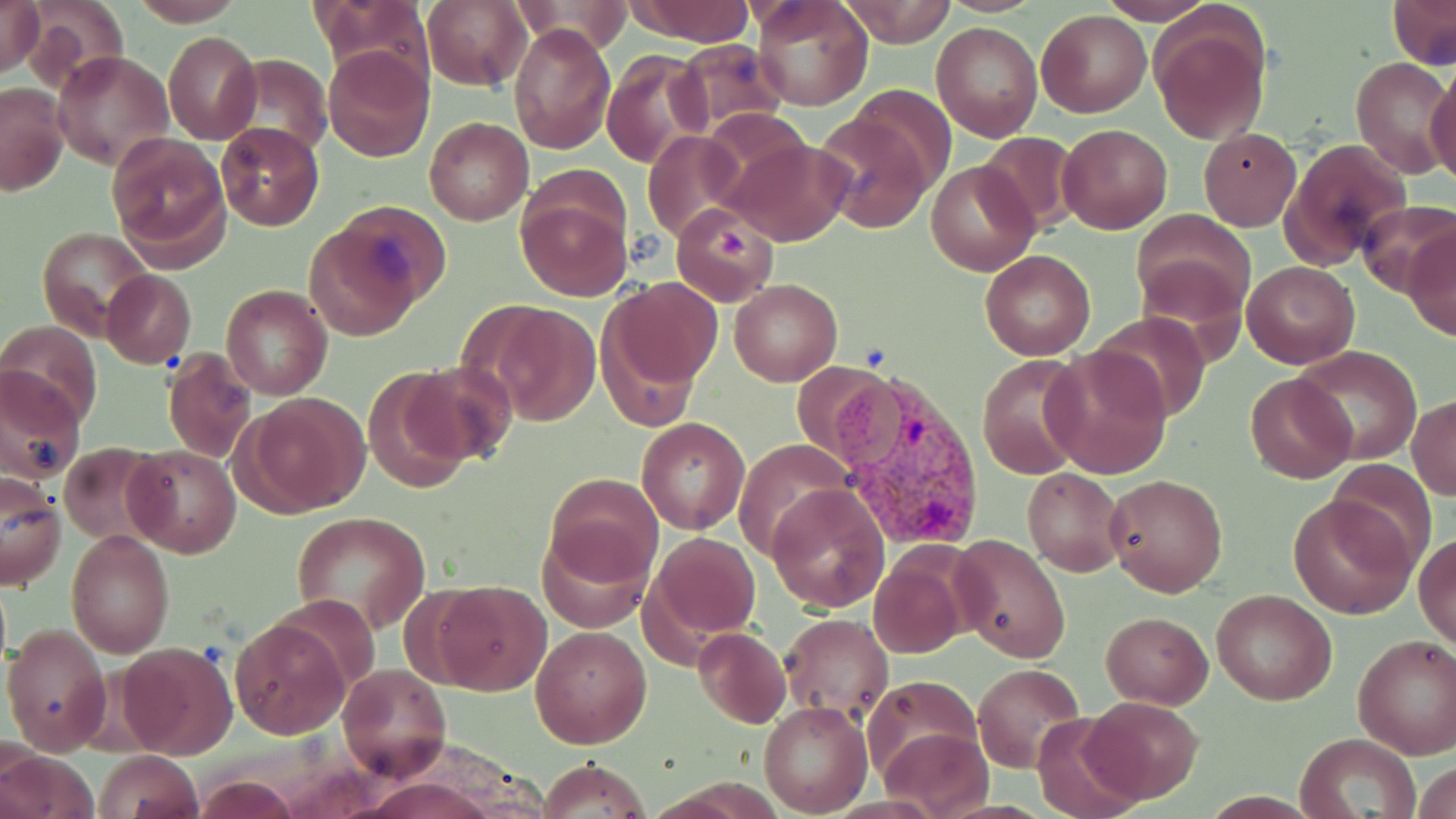
Summary:
  - Coordinate format: approximate bounding boxes as (x1, y1, x2, y2) in pixels
  - Uninfected red blood cell locations: (0, 0, 44, 79), (131, 0, 246, 25), (318, 0, 428, 84), (422, 0, 534, 92), (624, 0, 757, 45), (751, 0, 873, 112), (840, 0, 957, 47), (937, 0, 1043, 16), (1097, 0, 1218, 24), (1388, 0, 1455, 68), (507, 1, 637, 56), (23, 2, 128, 92), (1037, 9, 1152, 118), (1150, 13, 1270, 147), (932, 21, 1043, 141), (509, 22, 615, 155), (164, 31, 260, 143), (669, 39, 788, 132), (322, 44, 435, 162), (51, 49, 175, 171), (602, 49, 713, 170), (227, 54, 332, 158), (1350, 56, 1453, 178), (1426, 71, 1456, 189), (1, 84, 69, 196), (812, 110, 935, 233), (423, 117, 533, 225), (215, 122, 323, 232), (1057, 123, 1173, 235), (1199, 127, 1301, 229), (642, 129, 750, 243), (975, 131, 1080, 233), (107, 134, 230, 262), (724, 137, 853, 245), (1284, 138, 1411, 268), (927, 160, 1039, 276), (515, 175, 634, 302), (327, 200, 450, 314), (1356, 200, 1456, 298), (669, 206, 777, 305), (1130, 209, 1257, 323), (304, 226, 420, 340), (1403, 226, 1456, 342), (38, 228, 156, 338), (980, 249, 1096, 360), (1136, 254, 1247, 359), (1241, 259, 1360, 368), (101, 270, 196, 368), (603, 277, 724, 392), (731, 279, 842, 386), (222, 284, 332, 400), (475, 301, 602, 426), (1089, 310, 1212, 422), (0, 322, 102, 429), (1291, 344, 1423, 464), (1041, 347, 1173, 479), (161, 349, 255, 463), (977, 355, 1087, 478), (793, 361, 900, 465), (404, 362, 515, 466), (0, 366, 86, 484), (362, 368, 481, 492), (1245, 372, 1356, 484), (241, 392, 368, 515), (1409, 395, 1456, 501), (637, 417, 750, 535), (733, 438, 856, 562), (60, 442, 167, 547), (127, 445, 241, 558), (1324, 459, 1440, 571), (1023, 467, 1128, 575), (546, 473, 662, 581), (1105, 473, 1229, 596), (1, 476, 66, 592), (768, 485, 890, 612), (1288, 493, 1416, 619), (290, 511, 432, 630), (536, 522, 653, 633), (65, 531, 175, 658), (644, 531, 761, 646), (1415, 531, 1455, 652), (949, 533, 1073, 663), (868, 548, 971, 660), (433, 579, 552, 695), (1211, 589, 1337, 705), (1100, 611, 1212, 708), (779, 612, 893, 723), (229, 617, 351, 740), (3, 623, 114, 756), (530, 626, 651, 747), (692, 627, 791, 729), (1352, 634, 1456, 759), (119, 641, 238, 758), (973, 662, 1085, 775), (338, 664, 451, 781), (862, 675, 982, 782), (1081, 695, 1204, 804), (758, 701, 872, 816), (1031, 711, 1143, 819), (879, 727, 994, 819), (1296, 734, 1419, 819), (1, 749, 100, 819), (94, 750, 203, 819), (539, 758, 649, 818), (1414, 758, 1456, 819), (191, 772, 303, 817), (359, 777, 496, 818)
  - Plasmodium vivax-infected red blood cell locations: (820, 364, 992, 555)
  - Slide-level diagnosis: Plasmodium vivax
  - Modality: light microscopy
  - Stain: May-Grünwald-Giemsa
  - Image size: 1456×819 pixels
  - Preparation: thin blood film
  - Magnification: 1000x
  - Field of view: single